Describe the morphology of the red blood cells.
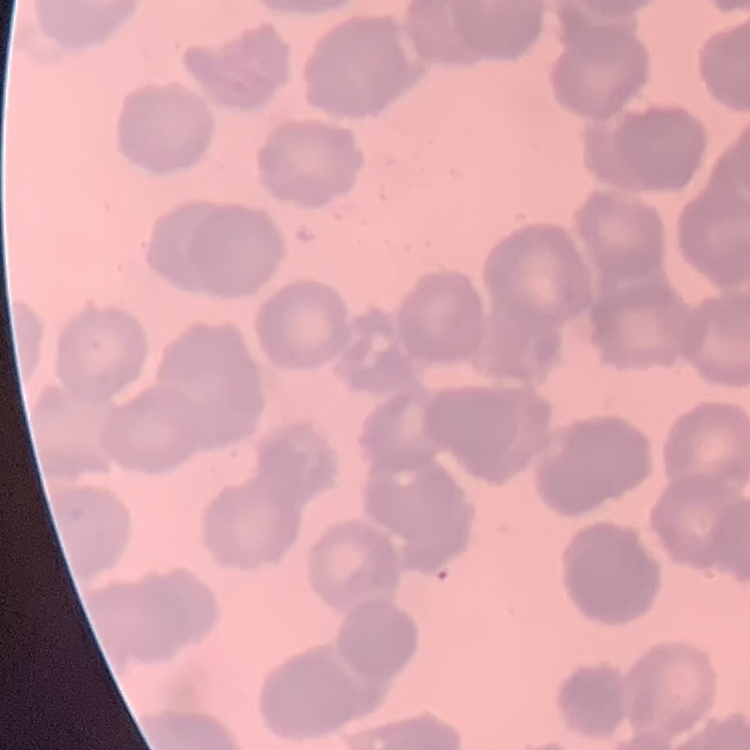
They show rouleaux formation.

Stained with either Field's or Giemsa. One tile cut from a larger photomicrograph. Thin blood film.